Report the malaria status of this cell.
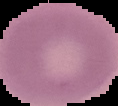

Uninfected.

From a thin blood film. Cell region segmented out of the field of view; the surrounding area is masked to black. Image is 118×106 pixels.